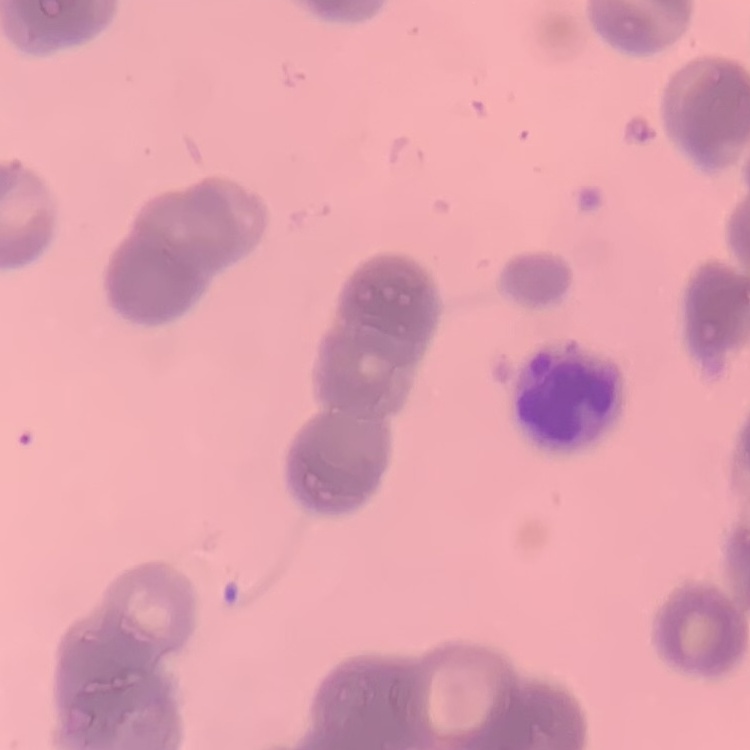
Summary:
  - Erythrocyte morphology: rouleaux formation
  - Stain: Field's or Giemsa
  - Image type: square crop of a larger photomicrograph
  - Preparation: thin blood smear